Report the malaria status of this cell.
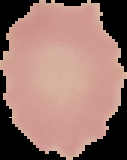

It is uninfected.

Summary:
  - Preparation: thin blood film
  - Image type: segmented cell region on a black background
  - Image size: 127×160 pixels